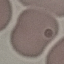
Result: no malaria parasites seen. Cell patch, automatically extracted from a larger field of view and resized to 64 × 64 pixels. Thin blood film. Acquired by smartphone through the microscope eyepiece. Giemsa stain.